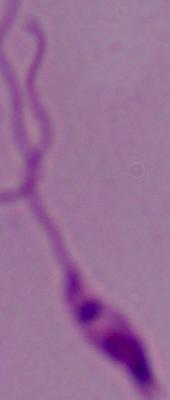 A Leishmania parasite is seen. 1000x magnification. Photomicrograph.